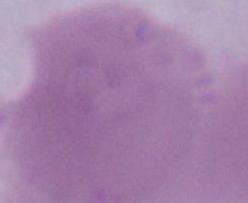
{
  "identification": "erythrocyte",
  "magnification": "1000x",
  "modality": "micrograph"
}